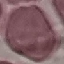 Result: no malaria parasites detected. Photographed with a smartphone camera at the microscope eyepiece. Giemsa stain. Automatically extracted cell patch, resized to 64 × 64 pixels. Thin smear of blood.